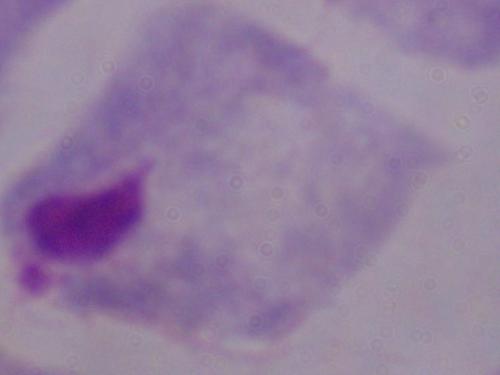
Summary:
  - Modality: photomicrograph
  - Magnification: 1000x
  - Identification: trichomonad